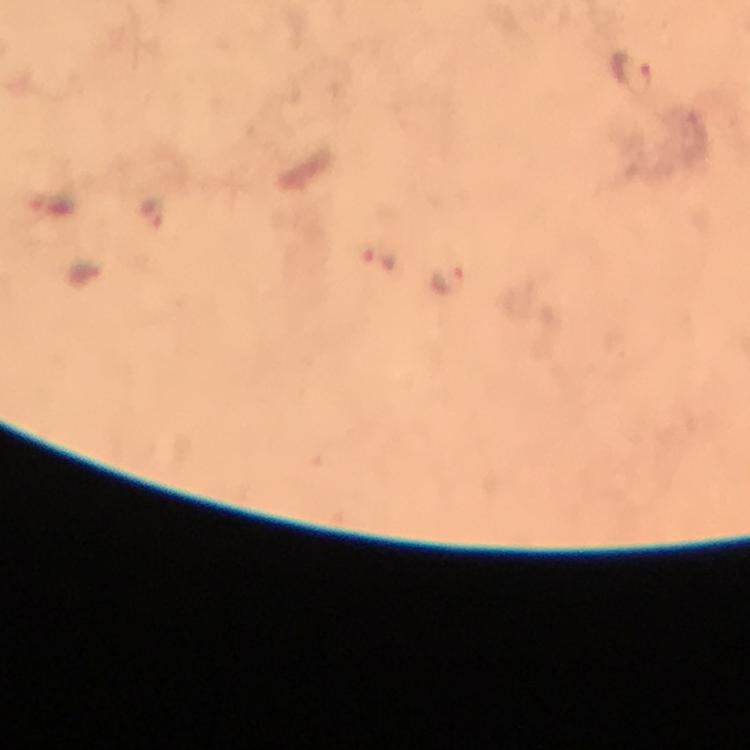
Approximate object centers, in pixels from the top-left corner. Malaria parasite locations: (x=632, y=76), (x=155, y=210), (x=379, y=257), (x=445, y=279). From a malaria diagnostic workup. At 100x magnification. Immersion oil was used. Giemsa-stained preparation. Cropped region of a single field of view. Image is 750×750 pixels. Photographed with a smartphone mounted on the microscope. Thick smear.